Name the parasite shown.
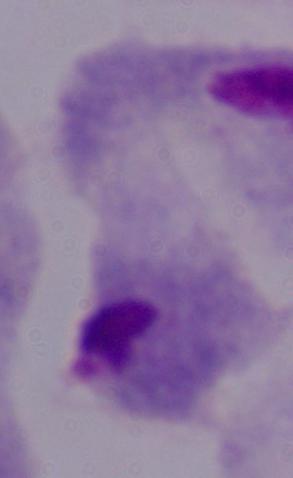
A trichomonad.

Summary:
  - Modality: photomicrograph
  - Magnification: 1000x